Outline each blood parasite and name the species.
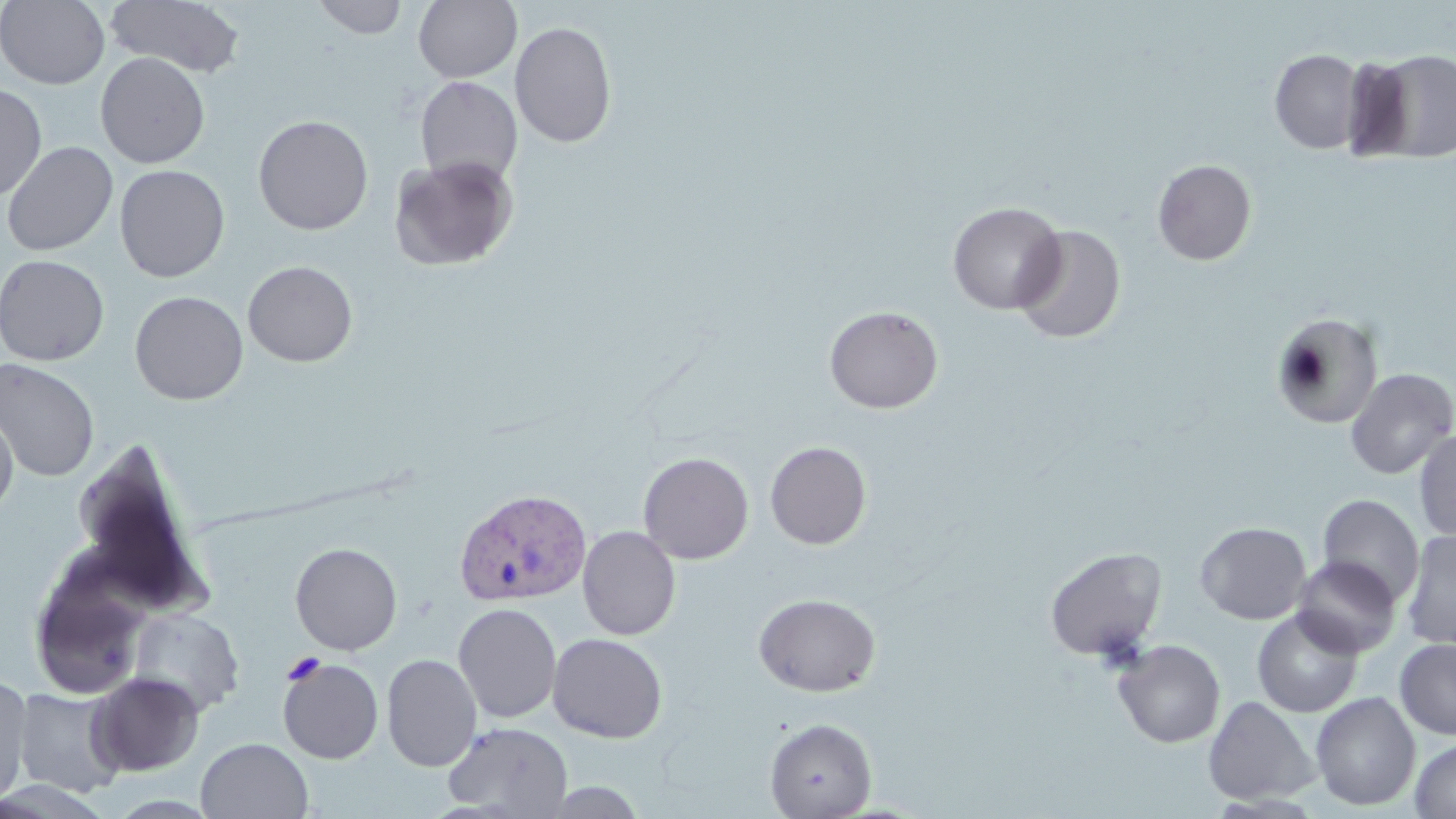
Approximate bounding boxes as (x1,y1)-(x2,y2) corner pairs in pixels.
Plasmodium vivax-infected red blood cells: (453,487)-(591,606).
No Plasmodium falciparum, Plasmodium ovale, Plasmodium malariae, Babesia divergens, or Trypanosoma brucei observed.

slide-level diagnosis = Plasmodium vivax
stain = May-Grünwald-Giemsa
preparation = thin blood smear
image size = 1456×819 pixels
modality = optical microscopy
uninfected red blood cell locations = approximate bounding boxes as (x1,y1)-(x2,y2) corner pairs in pixels: (0,0)-(110,90), (105,0)-(246,79), (312,0)-(409,39), (413,0)-(522,83), (510,21)-(617,149), (1362,48)-(1456,163), (1270,49)-(1366,154), (96,52)-(210,169), (106,52)-(218,284), (415,75)-(522,187), (0,83)-(47,201), (253,114)-(373,235), (2,140)-(118,256), (389,155)-(519,272), (1152,159)-(1256,266), (114,164)-(230,282), (947,201)-(1066,315), (1011,224)-(1127,344), (0,254)-(109,366), (242,260)-(358,367), (130,291)-(248,405), (824,305)-(944,414), (1271,312)-(1384,430), (0,358)-(100,481), (1344,367)-(1456,479), (0,405)-(18,520), (1413,428)-(1456,543), (765,441)-(872,550), (638,452)-(754,564), (1317,494)-(1424,607), (1195,521)-(1311,624), (578,525)-(680,640), (1401,529)-(1456,651), (290,542)-(402,655), (1044,547)-(1167,661), (29,555)-(154,701), (1292,555)-(1402,658), (753,593)-(881,697), (453,602)-(562,723), (127,608)-(244,717), (1252,608)-(1363,717), (547,632)-(668,743), (1395,638)-(1456,740), (1113,639)-(1225,748), (381,654)-(482,772), (278,657)-(384,764), (88,672)-(204,776), (0,674)-(31,807), (13,686)-(127,797), (1310,691)-(1421,811), (1202,695)-(1320,805), (764,718)-(877,819), (442,722)-(573,817), (196,737)-(313,819), (1410,737)-(1456,819), (539,781)-(650,818)
magnification = 1000x
field of view = one of a larger specimen